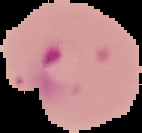

image_type: cell region segmented out of the field of view; surrounding area masked to black
malaria_status: parasitized
image_size: 142×133 pixels
preparation: thin blood film